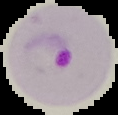
Malaria status: parasitized. Image is 118×115 pixels. The area outside the segmented cell region is set to black. From a thin blood smear.